Name the blood parasite species.
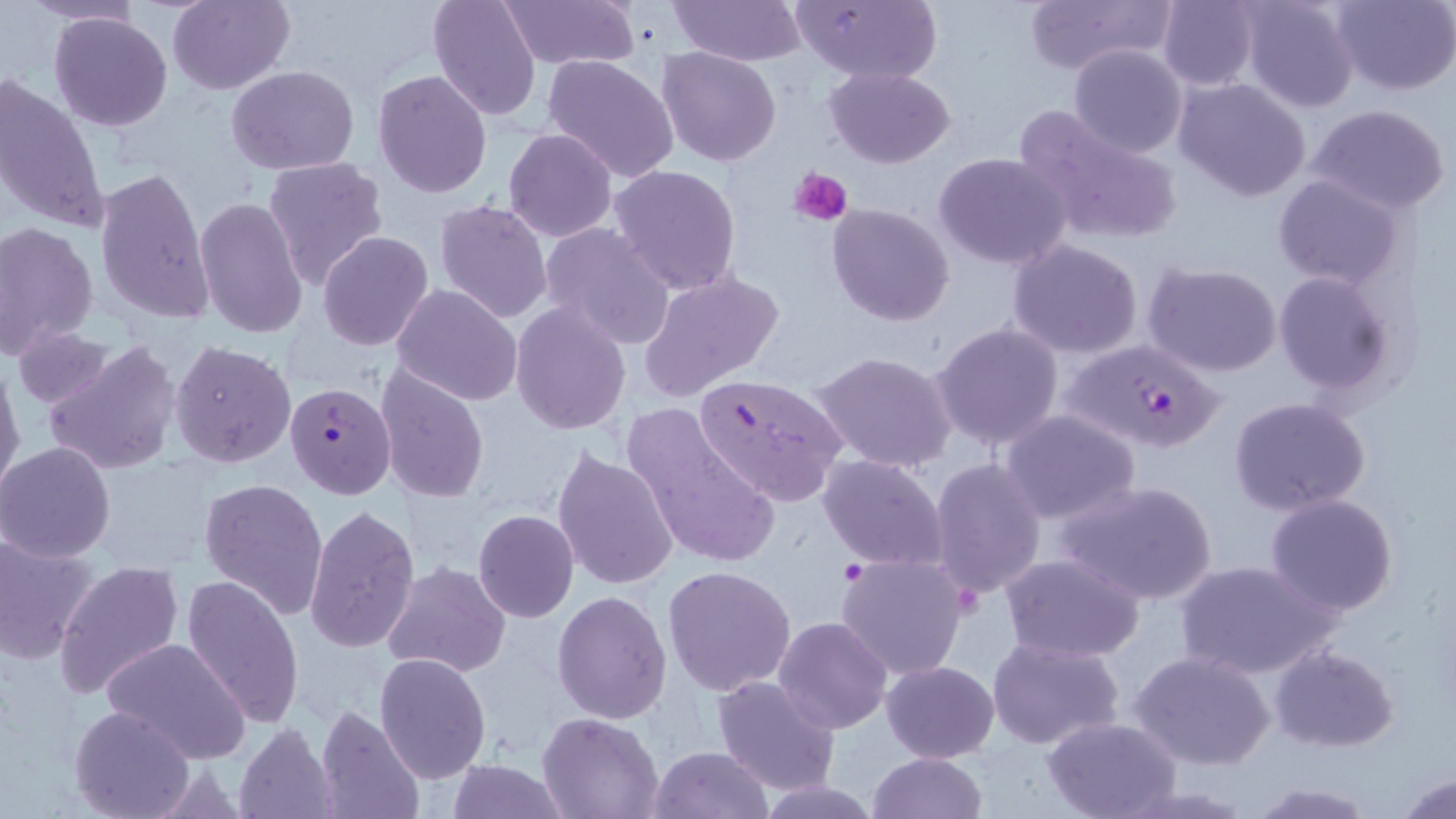
Plasmodium falciparum.

Approximate bounding boxes as [x1, y1, x2, y2] in pixels. Uninfected red blood cell locations (subset): [21, 0, 143, 27], [167, 0, 294, 94], [427, 0, 542, 120], [500, 0, 640, 72], [669, 0, 806, 67], [789, 0, 942, 87], [1022, 0, 1176, 77], [1157, 0, 1263, 90], [1239, 0, 1359, 113], [1331, 0, 1456, 95], [48, 11, 172, 131], [1069, 44, 1188, 158], [657, 47, 783, 166], [541, 54, 681, 184], [227, 63, 360, 175], [824, 66, 956, 167], [373, 69, 492, 197], [0, 73, 108, 238], [1174, 78, 1313, 204], [1012, 102, 1182, 248], [1308, 103, 1451, 216], [504, 129, 618, 241], [933, 152, 1072, 271], [261, 155, 389, 292], [609, 163, 743, 295], [94, 167, 217, 325], [1273, 174, 1403, 291], [195, 197, 309, 339], [433, 199, 553, 323], [826, 202, 955, 326], [0, 221, 98, 357], [538, 223, 676, 351], [318, 231, 434, 350], [1006, 237, 1144, 360], [1141, 262, 1283, 379], [641, 269, 785, 401], [1272, 271, 1399, 399], [392, 283, 523, 407], [510, 301, 632, 435], [929, 319, 1066, 451], [13, 326, 117, 411], [42, 339, 181, 477], [168, 340, 295, 468], [811, 350, 959, 475], [0, 362, 23, 495], [374, 366, 489, 505], [1228, 395, 1370, 516], [626, 404, 780, 573], [1000, 411, 1141, 526], [0, 441, 117, 563], [551, 448, 679, 593], [818, 453, 949, 571], [929, 455, 1047, 601], [199, 478, 329, 619], [1055, 478, 1219, 606], [1264, 493, 1399, 616], [303, 504, 420, 658], [472, 510, 579, 623], [0, 533, 101, 663], [836, 553, 970, 680], [1000, 553, 1146, 664], [1174, 559, 1336, 680], [54, 560, 185, 701], [381, 564, 510, 678], [663, 565, 796, 695], [181, 575, 304, 730], [552, 590, 671, 723], [773, 616, 892, 734], [987, 635, 1126, 751], [98, 636, 250, 765], [1269, 644, 1398, 752], [1130, 651, 1277, 771], [374, 653, 491, 783], [882, 661, 999, 761], [711, 673, 841, 794], [315, 703, 427, 819], [68, 706, 197, 819], [540, 713, 661, 819], [1042, 717, 1182, 819], [233, 722, 339, 818], [649, 745, 772, 819], [868, 752, 987, 819], [444, 760, 568, 818], [1394, 772, 1456, 818], [755, 778, 884, 818], [1247, 780, 1378, 818]. Plasmodium falciparum-infected red blood cell locations (subset): [1060, 339, 1224, 458], [693, 372, 850, 505]. Platelet locations: [789, 166, 853, 228]. Thin blood smear. 1000x magnification. Light microscopy. Image is 1456×819 pixels. May-Grünwald-Giemsa-stained preparation. Single field of view.